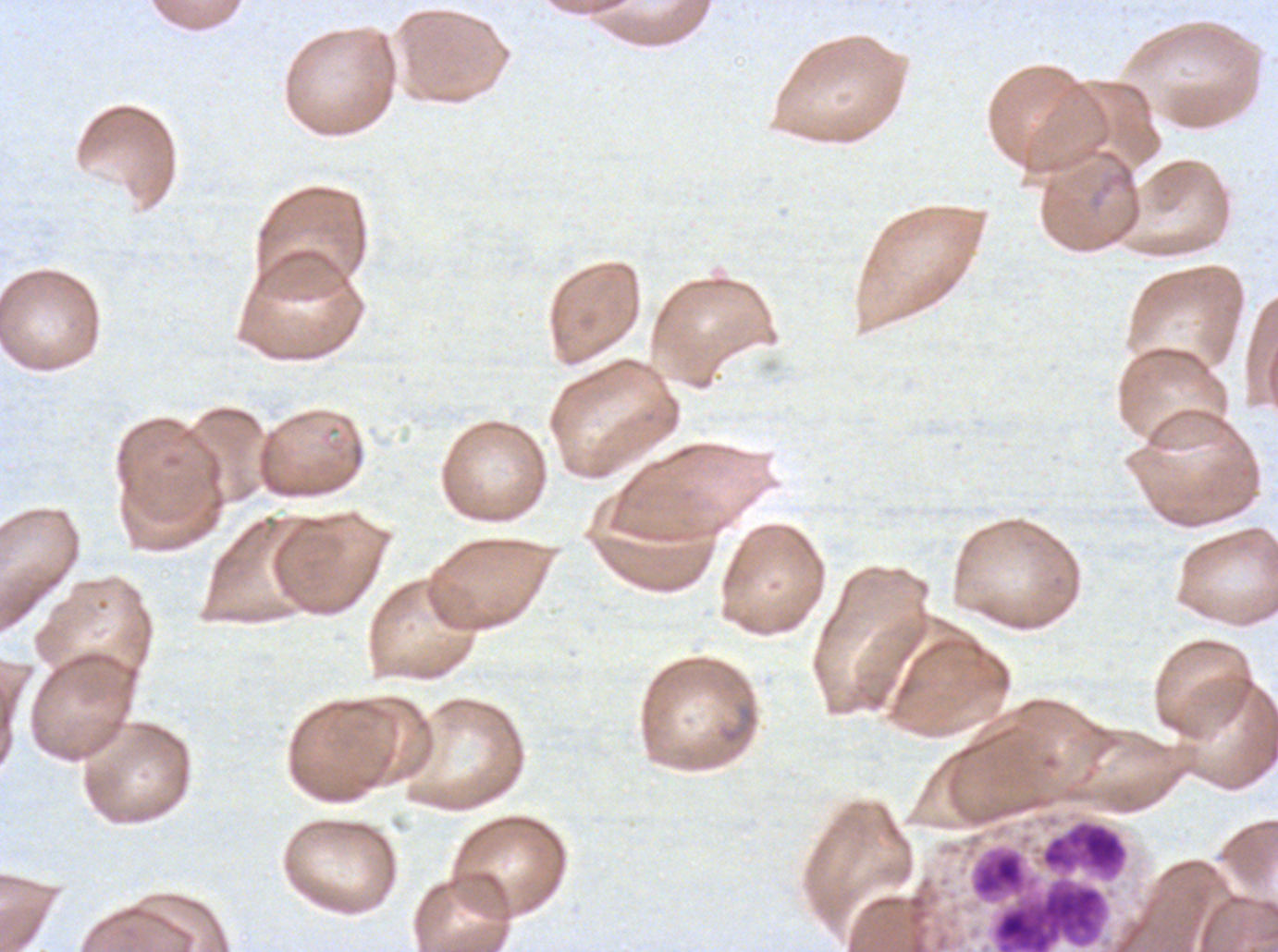

Approximate bounding boxes as {x1, y1, x2, y2} in pixels.
Summary:
  - Leukocyte locations: {993, 882, 1105, 951}
  - Field of view: sub-image separated from a larger composite
  - Stain: Giemsa
  - Specimen: P. falciparum from a patient in The Gambia, cultured ex vivo for 24 to 48 hours
  - Preparation: thin blood smear
  - Image size: 1278×952 pixels